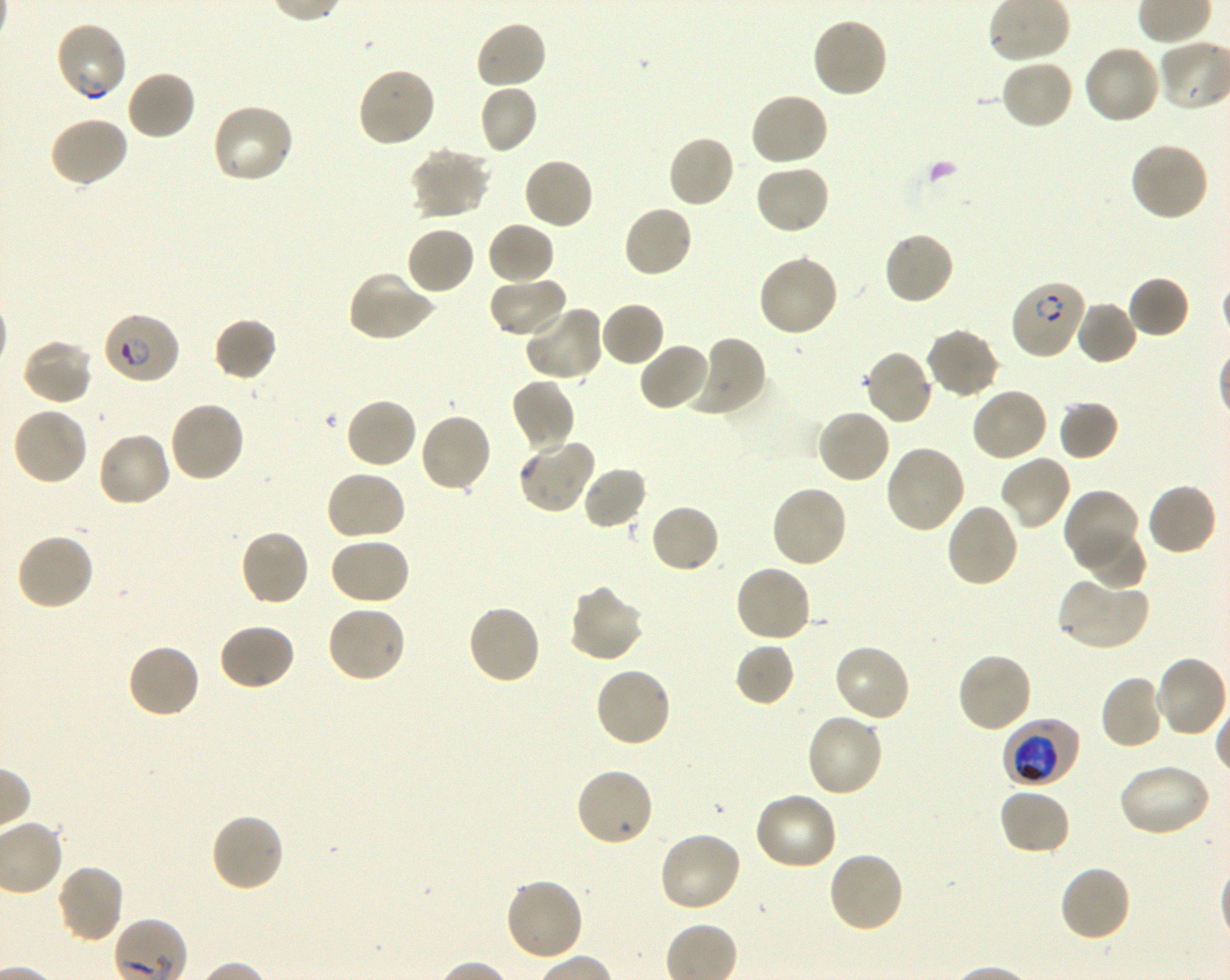 Approximate bounding boxes as {x1, y1, x2, y2} in pixels. Not every red blood cell is marked. A life-cycle stage — or a range of stages, where the recorded stages span more than one — follows each staged infected red blood cell. Locations of uninfected red blood cells: {811, 17, 888, 100}, {475, 20, 548, 91}, {1082, 43, 1163, 124}, {999, 57, 1074, 131}, {357, 66, 437, 148}, {126, 69, 197, 140}, {479, 84, 538, 155}, {748, 92, 829, 168}, {210, 101, 295, 185}, {47, 115, 129, 189}, {666, 134, 736, 209}, {1129, 140, 1210, 222}, {409, 147, 493, 220}, {522, 156, 594, 231}, {754, 163, 830, 236}, {622, 203, 694, 279}, {486, 221, 556, 287}, {405, 224, 476, 296}, {882, 230, 955, 306}, {755, 254, 839, 338}, {347, 269, 436, 342}, {488, 275, 569, 339}, {1128, 276, 1190, 339}, {1074, 300, 1138, 366}, {600, 301, 666, 368}, {523, 304, 605, 383}, {212, 316, 278, 382}, {925, 327, 1001, 399}, {686, 335, 768, 418}, {21, 338, 95, 406}, {638, 342, 711, 412}, {863, 348, 935, 427}, {509, 377, 577, 454}, {970, 387, 1048, 463}, {344, 397, 418, 470}, {1057, 399, 1119, 461}, {168, 400, 246, 483}, {11, 405, 89, 487}, {816, 407, 892, 485}, {418, 413, 493, 494}, {95, 431, 172, 508}, {517, 437, 595, 515}, {884, 444, 966, 535}, {998, 454, 1073, 532}, {581, 465, 648, 531}, {325, 469, 407, 542}, {1146, 482, 1218, 557}, {769, 484, 848, 570}, {1063, 487, 1141, 566}, {945, 502, 1020, 589}, {649, 503, 720, 574}, {238, 528, 310, 608}, {1079, 528, 1147, 589}, {15, 532, 95, 612}, {328, 537, 411, 606}, {734, 563, 812, 644}, {1056, 579, 1149, 652}, {565, 583, 645, 663}, {466, 603, 543, 686}, {325, 604, 408, 684}, {217, 623, 296, 692}, {126, 642, 202, 719}, {735, 642, 795, 707}, {833, 642, 912, 724}, {956, 651, 1034, 733}, {1154, 655, 1229, 739}, {593, 666, 672, 749}, {1099, 674, 1165, 750}, {805, 712, 885, 798}, {1116, 762, 1212, 837}, {574, 767, 654, 849}, {998, 786, 1073, 856}, {754, 790, 839, 871}, {210, 812, 286, 893}, {657, 830, 742, 913}, {827, 850, 906, 934}, {55, 863, 126, 944}, {1057, 864, 1131, 944}, {503, 877, 585, 963}. Locations of infected red blood cells: {54, 21, 129, 103}; {1010, 278, 1087, 359} ring; {102, 312, 181, 385} ring; {1003, 718, 1080, 787} trophozoite. Life-cycle stages observed: ring, trophozoite. Plasmodium falciparum strain 3D7 in shaking in-vitro culture. Giemsa stain. Thin blood smear. 100x objective under oil immersion, numerical aperture 1.30. Donor blood group O+. Image is 1230×980 pixels. One field from this slide.